Comment on the morphology of the red blood cells.
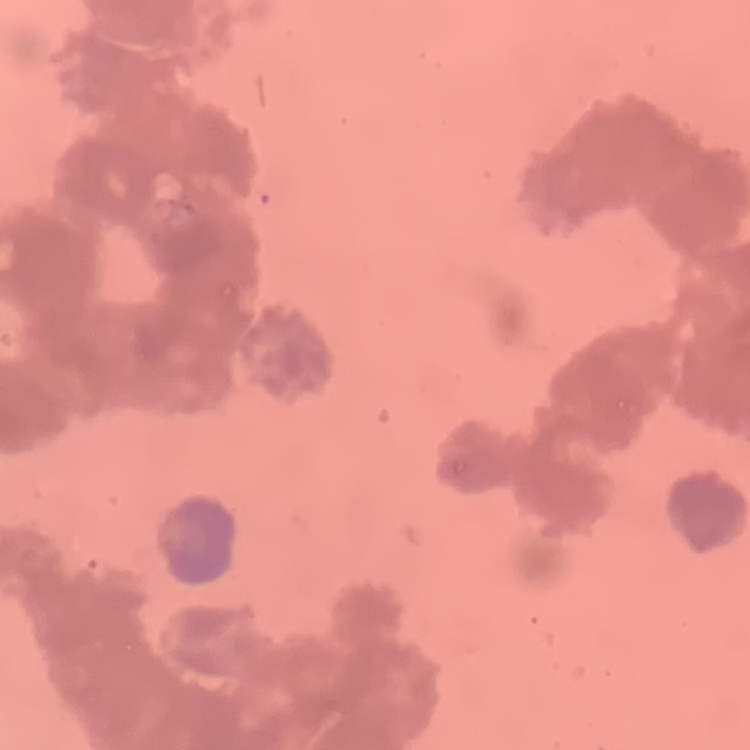
They show rouleaux formation.

{
  "preparation": "thin peripheral smear",
  "image_type": "one tile cut from a larger photomicrograph",
  "stain": "Field's or Giemsa"
}